Give the position of every Plasmodium parasite visible.
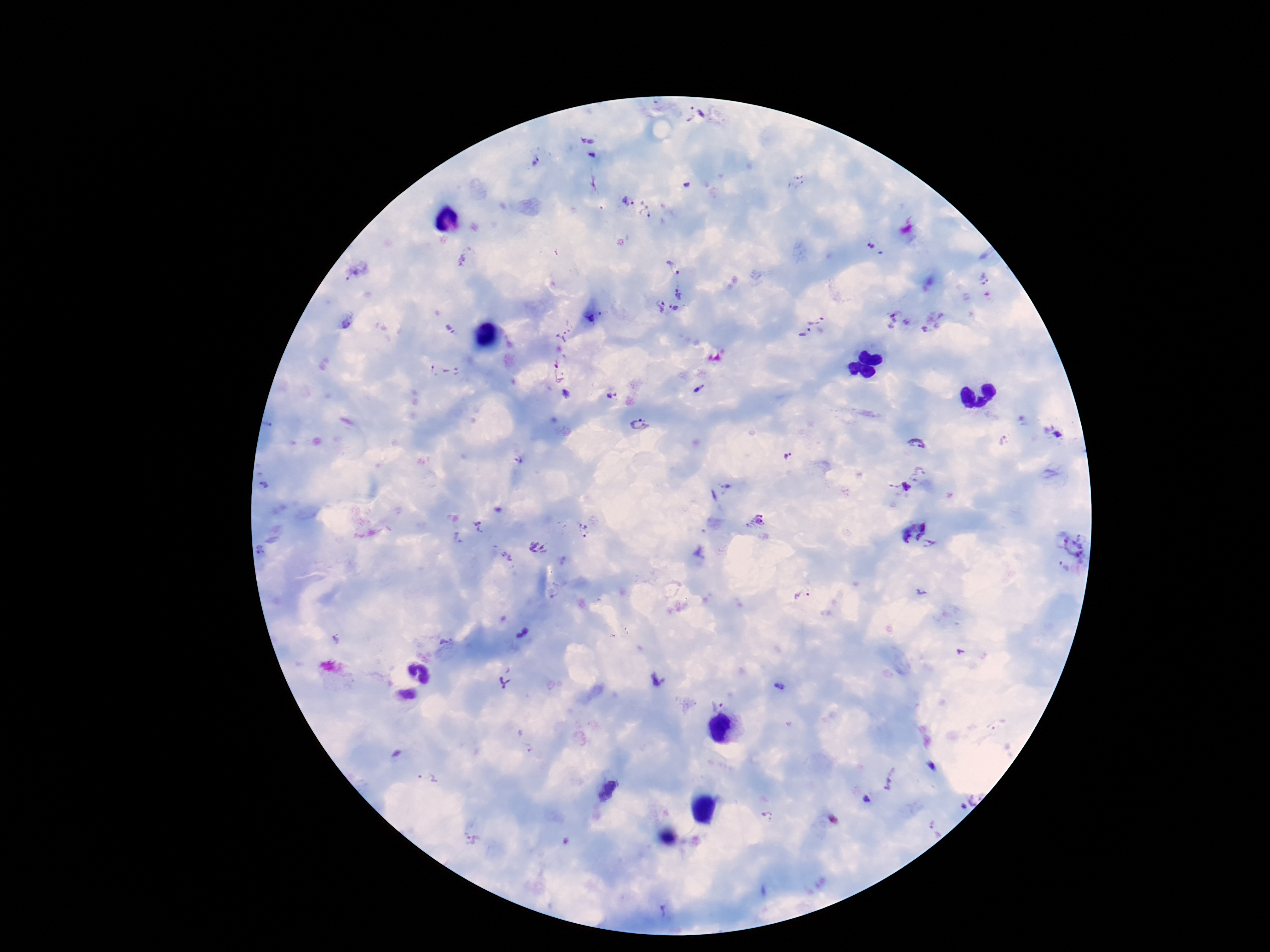
Approximate centers as {x, y} in pixels.
Plasmodium parasites: {694, 114}, {587, 141}, {593, 155}, {535, 159}, {797, 182}, {689, 184}, {625, 202}, {647, 211}, {872, 245}, {674, 268}, {356, 271}, {985, 279}, {678, 292}, {655, 306}, {673, 309}, {596, 317}, {817, 317}, {892, 320}, {571, 324}, {925, 329}, {453, 330}, {804, 335}, {560, 337}, {431, 370}, {451, 373}, {557, 377}, {699, 389}, {566, 394}, {612, 395}, {639, 425}, {1004, 441}, {918, 443}, {788, 456}, {518, 461}, {919, 474}, {266, 485}, {725, 486}, {897, 489}, {756, 522}, {480, 527}, {584, 530}, {911, 530}, {460, 538}, {1075, 543}, {932, 545}, {538, 549}, {263, 550}, {507, 559}, {1063, 566}, {803, 599}, {523, 633}, {446, 643}, {658, 680}, {505, 683}, {780, 687}, {714, 702}, {608, 790}, {868, 800}.

Summary:
  - Stain: Giemsa
  - Capture: smartphone camera through the microscope eyepiece
  - Image size: 1270×952 pixels
  - Patient malaria status: infected
  - Field of view: single
  - Preparation: thick blood film
  - Magnification: 100x